Report the malaria status of this cell.
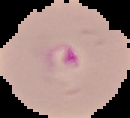

It is parasitized.

Segmented cell region on a black background. Image is 130×118 pixels. From a thin blood film.